Locate every blood parasite and identify its species.
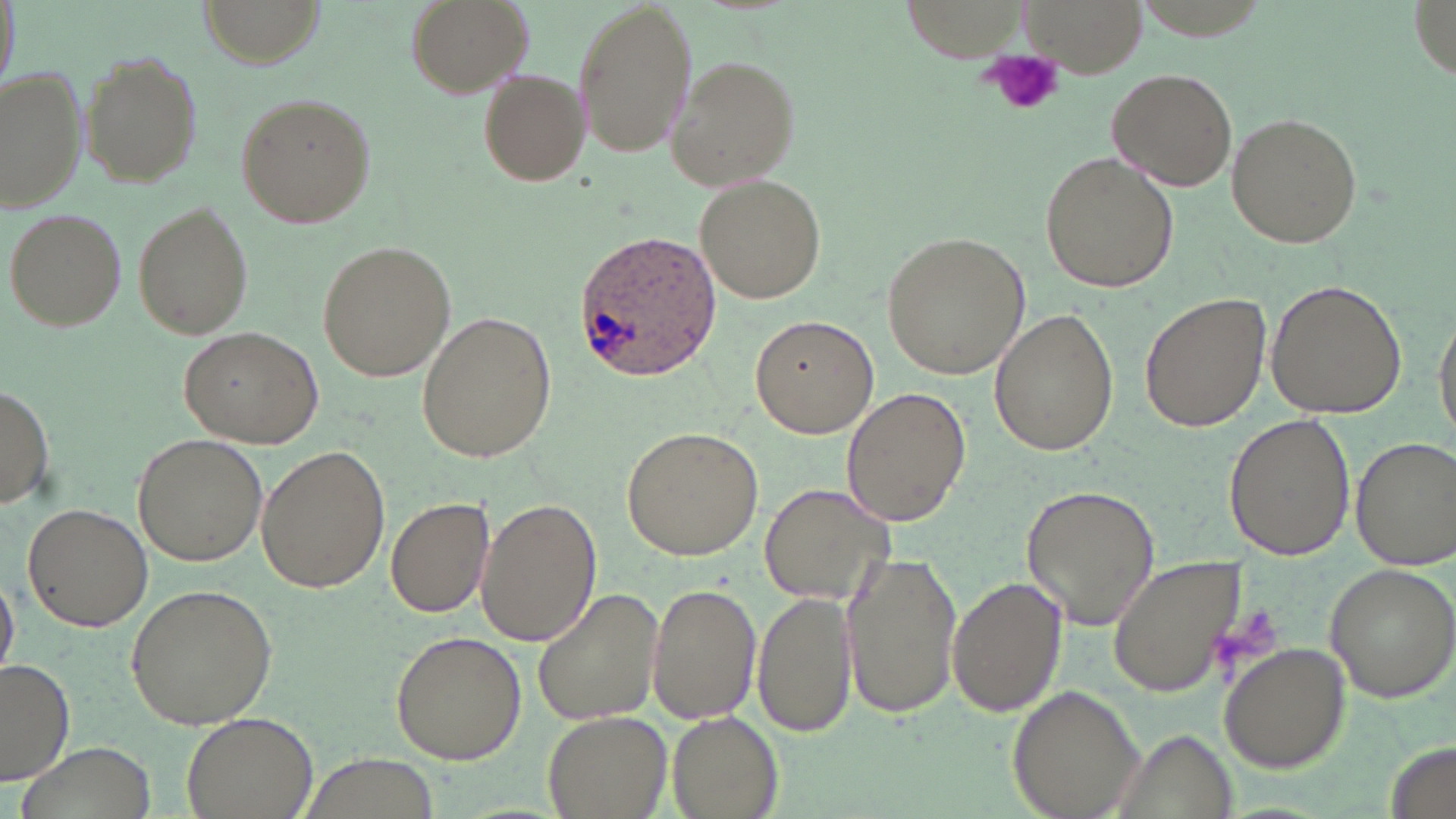

Approximate bounding boxes as (x1, y1, x2, y2) in pixels.
Plasmodium ovale-infected red blood cells: (570, 229, 724, 384).
No Plasmodium falciparum, Plasmodium malariae, Plasmodium vivax, Babesia divergens, or Trypanosoma brucei observed.

slide-level diagnosis = Plasmodium ovale
magnification = 1000x
field of view = one of a larger specimen
stain = May-Grünwald-Giemsa
platelet locations = approximate bounding boxes as (x1, y1, x2, y2) in pixels: (989, 51, 1063, 114), (1212, 604, 1285, 672)
preparation = thin blood smear
modality = optical microscopy
image size = 1456×819 pixels
uninfected red blood cell locations = approximate bounding boxes as (x1, y1, x2, y2) in pixels: (404, 0, 533, 98), (572, 0, 697, 159), (1021, 0, 1144, 75), (201, 1, 323, 66), (78, 48, 204, 187), (666, 55, 802, 188), (3, 68, 87, 211), (477, 68, 589, 188), (1107, 68, 1239, 190), (234, 92, 375, 231), (1226, 112, 1363, 250), (1038, 151, 1179, 295), (695, 174, 824, 304), (133, 204, 252, 339), (5, 207, 127, 331), (884, 231, 1031, 379), (318, 240, 455, 383), (1267, 279, 1405, 418), (1139, 292, 1271, 436), (1431, 301, 1456, 449), (990, 309, 1116, 454), (415, 310, 556, 463), (749, 314, 878, 439), (178, 326, 323, 448), (0, 385, 53, 510), (840, 387, 970, 526), (1225, 413, 1353, 561), (621, 427, 764, 559), (132, 432, 267, 568), (1350, 435, 1455, 571), (257, 446, 391, 593), (760, 482, 897, 607), (1022, 486, 1160, 630), (385, 494, 495, 618), (477, 497, 600, 646), (21, 502, 152, 632), (841, 552, 964, 720), (1106, 553, 1246, 698), (1322, 562, 1456, 701), (0, 564, 19, 683), (949, 575, 1066, 717), (645, 581, 760, 726), (121, 583, 278, 731), (534, 587, 665, 727), (753, 591, 858, 738), (392, 630, 526, 764), (1219, 642, 1351, 772), (1, 659, 75, 786), (1009, 684, 1146, 818), (544, 709, 672, 818), (666, 710, 782, 818), (180, 712, 316, 818), (1107, 729, 1238, 818), (18, 741, 156, 819)